Identify the blood parasite species.
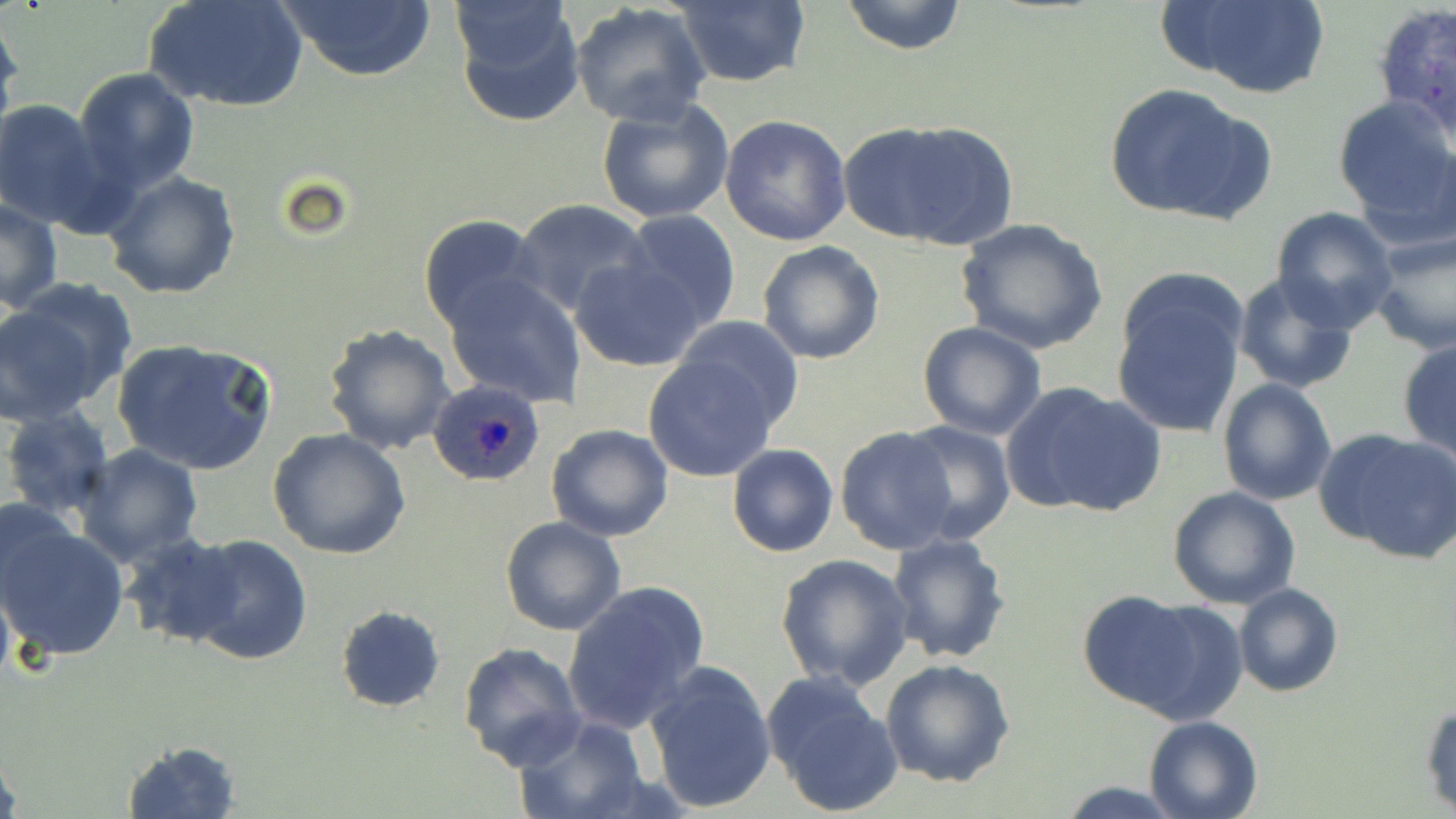

Plasmodium ovale.

preparation = thin blood smear
Plasmodium ovale-infected red blood cell locations = approximate bounding boxes as (x1,y1)-(x2,y2) corner pairs in pixels: (424,378)-(548,487)
image size = 1456×819 pixels
modality = optical microscopy
field of view = single
stain = May-Grünwald-Giemsa
uninfected red blood cell locations = approximate bounding boxes as (x1,y1)-(x2,y2) corner pairs in pixels: (147,0)-(307,114), (273,0)-(438,82), (451,0)-(585,128), (840,0)-(968,56), (1167,0)-(1334,100), (671,1)-(811,88), (570,2)-(711,127), (1369,4)-(1456,139), (0,16)-(22,136), (72,68)-(200,199), (1104,83)-(1272,225), (1332,95)-(1456,233), (595,98)-(733,224), (0,99)-(111,229), (721,114)-(853,246), (839,120)-(1016,249), (104,171)-(240,300), (1,196)-(63,314), (514,199)-(652,319), (1270,206)-(1397,329), (619,211)-(740,329), (418,213)-(547,337), (958,220)-(1106,356), (1366,230)-(1456,354), (757,239)-(885,364), (571,256)-(705,373), (1111,271)-(1248,442), (1231,271)-(1361,395), (442,273)-(588,408), (0,284)-(130,418), (677,315)-(804,433), (321,322)-(455,456), (917,322)-(1048,440), (1397,334)-(1456,464), (111,338)-(277,476), (641,351)-(783,482), (1217,377)-(1337,505), (1003,382)-(1166,517), (1,405)-(116,521), (899,419)-(1016,545), (545,423)-(674,543), (834,426)-(960,556), (1317,427)-(1456,559), (267,428)-(411,560), (727,443)-(839,559), (72,444)-(204,568), (1167,487)-(1300,610), (1,512)-(130,662), (500,517)-(627,637), (119,532)-(247,646), (180,533)-(312,666), (887,533)-(1012,665), (773,553)-(916,691), (562,580)-(709,736), (1233,583)-(1344,697), (1076,592)-(1221,719), (334,604)-(446,713), (458,642)-(586,771), (880,660)-(1017,788), (643,661)-(777,814), (761,669)-(903,817), (1421,697)-(1455,815), (513,715)-(649,819), (1143,715)-(1265,819), (119,739)-(242,818), (0,741)-(21,819), (1054,780)-(1183,818)
magnification = 1000x